Classify this cell by malaria status.
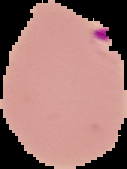
It is parasitized.

The area outside the segmented cell region is set to black. Image is 127×169 pixels. From a thin blood film.